Assess this cell for malaria.
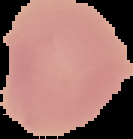

Uninfected.

Summary:
  - Image size: 133×139 pixels
  - Preparation: thin blood smear
  - Image type: segmented cell region on a black background